Outline each blood parasite and name the species.
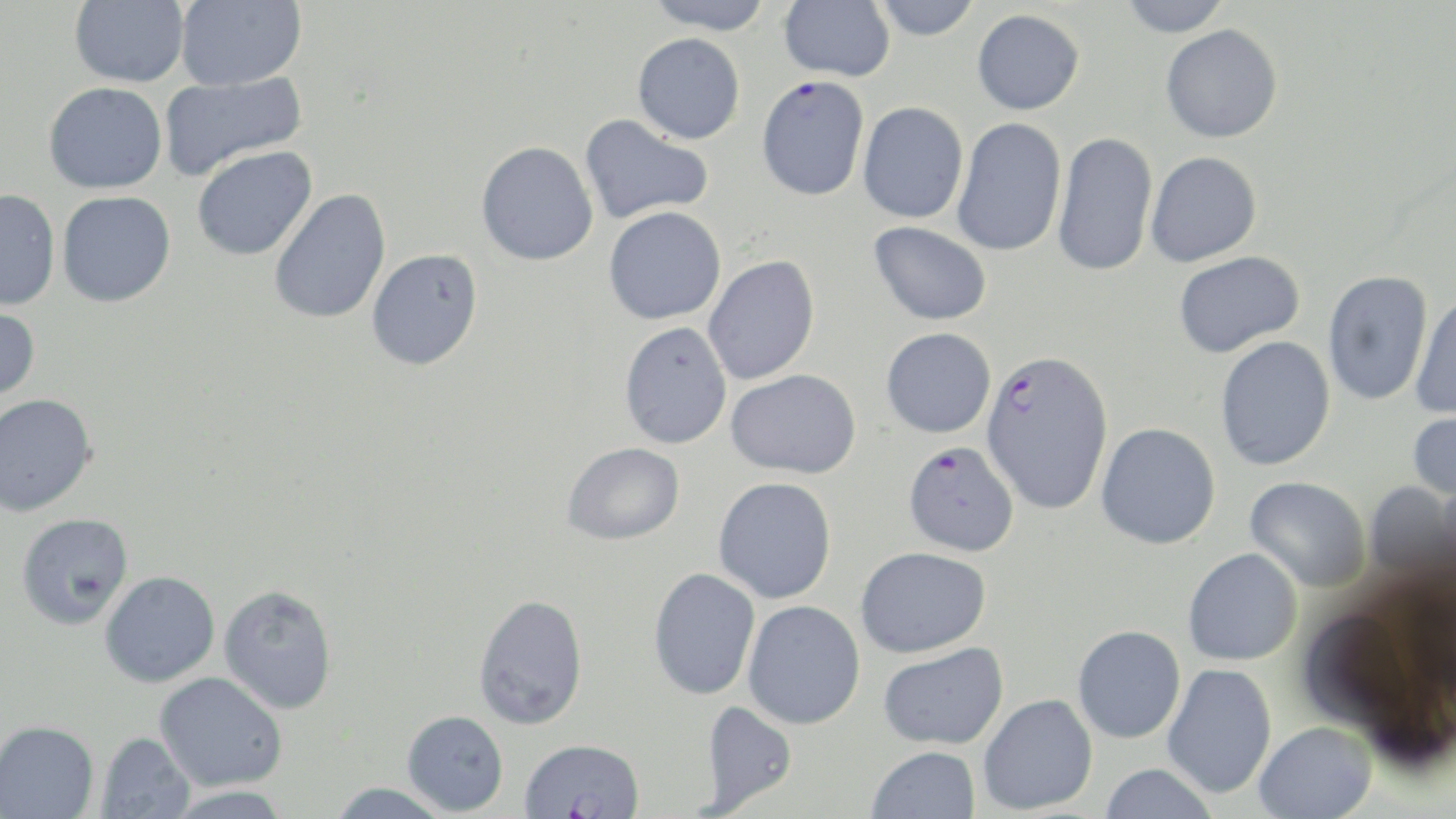
Approximate bounding boxes as [x1, y1, x2, y2] in pixels.
Plasmodium falciparum-infected red blood cells: [981, 349, 1113, 515], [902, 440, 1019, 556].
No Plasmodium ovale, Plasmodium malariae, Plasmodium vivax, Babesia divergens, or Trypanosoma brucei observed.

Summary:
  - Uninfected red blood cell locations: [69, 0, 189, 87], [175, 0, 306, 90], [643, 0, 777, 34], [778, 0, 896, 81], [872, 0, 982, 40], [1118, 0, 1233, 37], [972, 9, 1085, 115], [1160, 24, 1283, 142], [632, 33, 746, 144], [158, 72, 307, 181], [756, 75, 870, 201], [43, 81, 167, 194], [857, 101, 968, 224], [579, 114, 714, 225], [951, 117, 1067, 256], [1053, 131, 1158, 276], [476, 141, 599, 265], [192, 146, 317, 261], [1145, 151, 1262, 267], [0, 188, 60, 311], [269, 189, 391, 324], [56, 191, 176, 308], [603, 206, 726, 324], [869, 221, 992, 325], [366, 248, 483, 371], [1173, 251, 1305, 357], [703, 255, 820, 386], [1322, 270, 1434, 405], [1410, 291, 1456, 421], [0, 302, 41, 405], [618, 321, 732, 449], [881, 327, 996, 438], [1215, 335, 1336, 471], [726, 368, 862, 478], [0, 393, 98, 517], [1408, 406, 1456, 503], [1095, 422, 1221, 549], [562, 442, 685, 545], [713, 476, 837, 604], [1245, 476, 1371, 593], [1365, 481, 1456, 586], [15, 512, 134, 630], [855, 546, 991, 657], [1183, 547, 1303, 665], [648, 568, 761, 700], [99, 571, 220, 688], [218, 584, 338, 714], [473, 592, 588, 730], [743, 600, 866, 729], [1072, 625, 1186, 744], [878, 642, 1007, 749], [1162, 663, 1277, 799], [154, 671, 287, 791], [978, 693, 1098, 815], [699, 700, 798, 813], [402, 710, 509, 815], [0, 719, 99, 818], [1255, 721, 1377, 819], [96, 731, 196, 819], [519, 738, 644, 819], [866, 746, 980, 819], [1100, 763, 1218, 819], [327, 782, 452, 819], [161, 784, 295, 818]
  - Slide-level diagnosis: Plasmodium falciparum
  - Field of view: one of a larger specimen
  - Preparation: thin blood smear
  - Magnification: 1000x
  - Modality: light microscopy
  - Stain: May-Grünwald-Giemsa
  - Image size: 1456×819 pixels